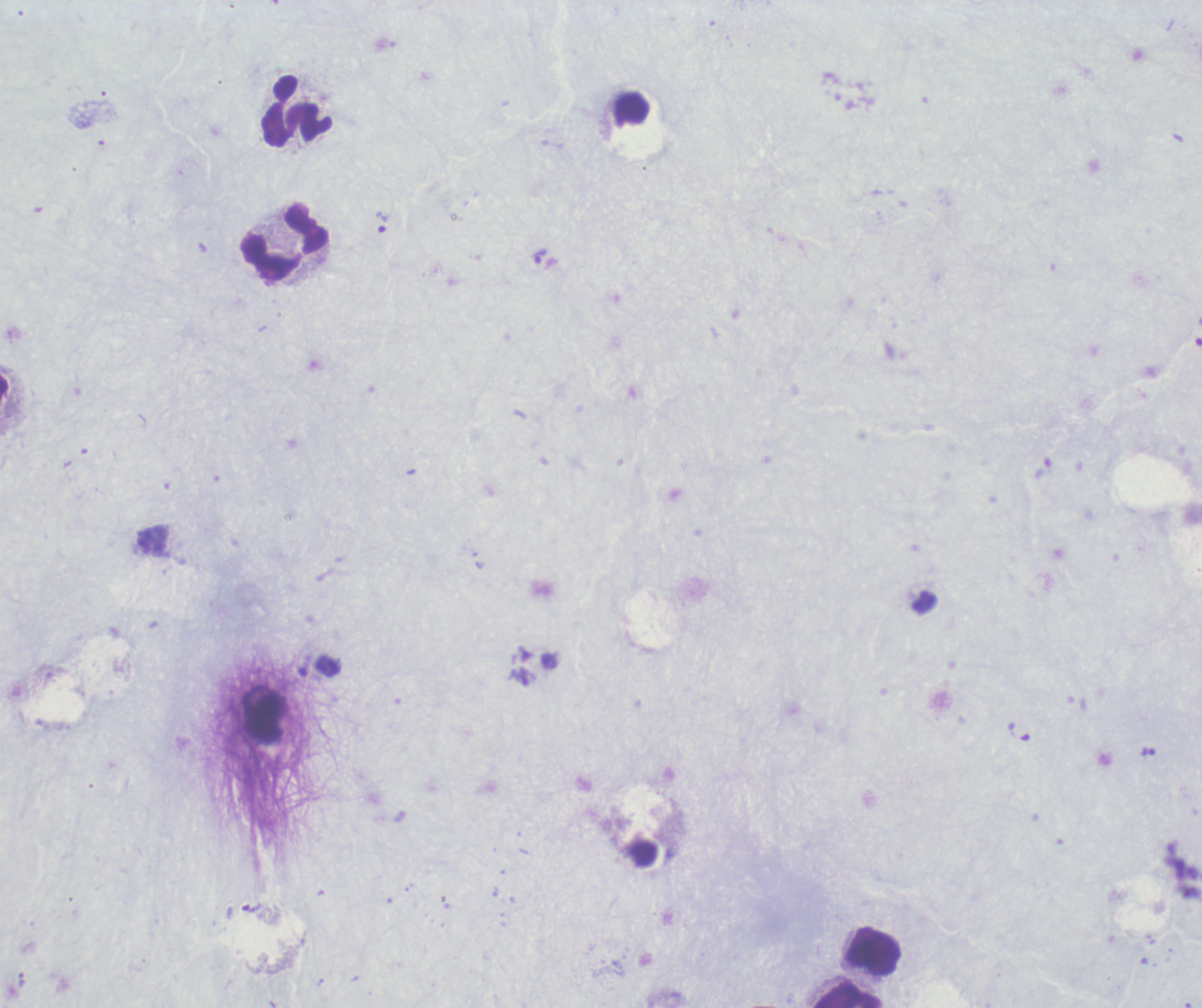
Approximate centers as {x, y} in pixels.
Summary:
  - Leukocyte locations: {298, 112}, {285, 243}, {874, 952}, {849, 995}
  - Trophozoite locations: {382, 222}, {540, 256}, {1149, 752}, {251, 908}
  - Stain: Romanowsky
  - Context: previously used in a real diagnosis
  - Preparation: thick blood smear
  - Magnification: 100x
  - Result: Plasmodium parasites identified
  - Background quality: unsatisfactory
  - Field of view: single
  - Image size: 1202×1008 pixels